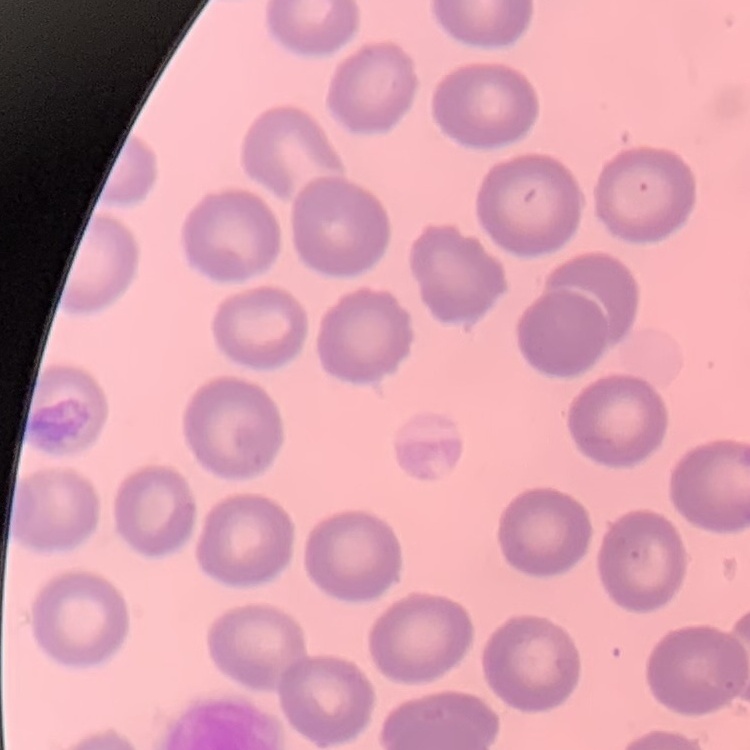

red blood cell morphology = no rouleaux formation
image type = one tile cut from a larger photomicrograph
stain = Field's or Giemsa
preparation = thin blood smear